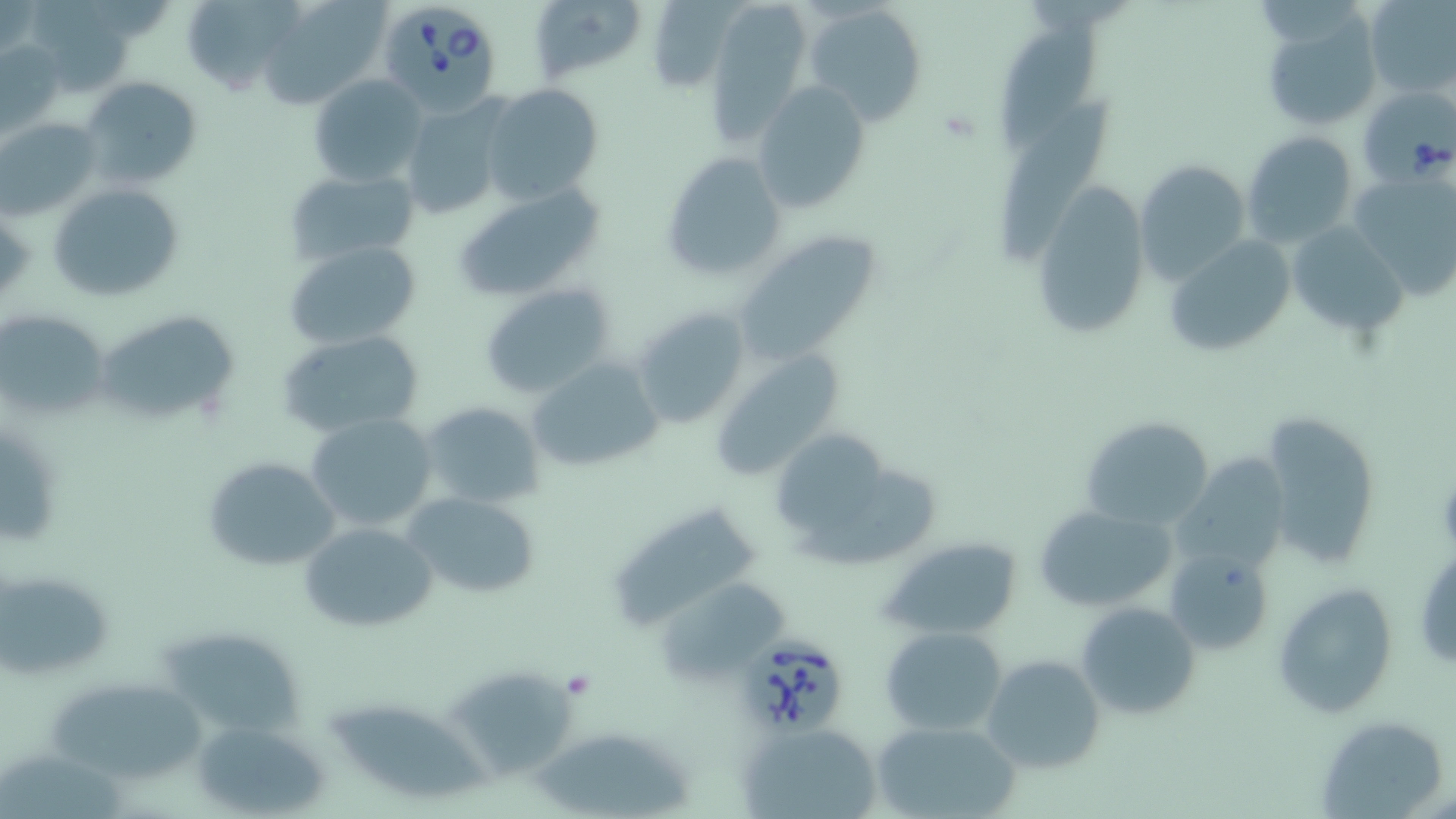

{
  "slide_level_diagnosis": "Babesia divergens",
  "uninfected_red_blood_cell_locations": "approximate bounding boxes as named x1/y1/x2/y2 corners in pixels: (x1=180, y1=0, x2=301, y2=98), (x1=259, y1=0, x2=388, y2=108), (x1=532, y1=0, x2=649, y2=80), (x1=649, y1=0, x2=732, y2=92), (x1=717, y1=0, x2=802, y2=143), (x1=1364, y1=1, x2=1453, y2=99), (x1=805, y1=4, x2=928, y2=128), (x1=1261, y1=11, x2=1383, y2=129), (x1=998, y1=16, x2=1100, y2=149), (x1=2, y1=40, x2=65, y2=133), (x1=306, y1=72, x2=429, y2=186), (x1=80, y1=76, x2=202, y2=188), (x1=753, y1=81, x2=873, y2=214), (x1=479, y1=84, x2=604, y2=206), (x1=1002, y1=96, x2=1116, y2=270), (x1=400, y1=97, x2=512, y2=221), (x1=1, y1=117, x2=100, y2=218), (x1=1242, y1=132, x2=1358, y2=248), (x1=659, y1=152, x2=786, y2=283), (x1=1133, y1=159, x2=1250, y2=284), (x1=1347, y1=167, x2=1456, y2=302), (x1=284, y1=168, x2=419, y2=265), (x1=1031, y1=178, x2=1150, y2=338), (x1=48, y1=180, x2=187, y2=302), (x1=453, y1=182, x2=610, y2=303), (x1=1287, y1=222, x2=1408, y2=338), (x1=733, y1=234, x2=882, y2=366), (x1=1164, y1=234, x2=1296, y2=359), (x1=283, y1=240, x2=419, y2=350), (x1=480, y1=283, x2=615, y2=399), (x1=631, y1=306, x2=752, y2=430), (x1=2, y1=310, x2=108, y2=419), (x1=100, y1=311, x2=239, y2=425), (x1=278, y1=329, x2=425, y2=436), (x1=707, y1=348, x2=848, y2=483), (x1=527, y1=357, x2=663, y2=475), (x1=419, y1=401, x2=549, y2=509), (x1=1258, y1=411, x2=1382, y2=570), (x1=306, y1=412, x2=440, y2=532), (x1=1080, y1=416, x2=1215, y2=530), (x1=778, y1=427, x2=884, y2=531), (x1=201, y1=455, x2=342, y2=572), (x1=1174, y1=455, x2=1291, y2=571), (x1=796, y1=478, x2=945, y2=570), (x1=401, y1=492, x2=542, y2=599), (x1=1032, y1=504, x2=1178, y2=613), (x1=612, y1=509, x2=757, y2=632), (x1=298, y1=522, x2=438, y2=633), (x1=882, y1=538, x2=1027, y2=639), (x1=1167, y1=549, x2=1275, y2=657), (x1=1, y1=571, x2=114, y2=676), (x1=1271, y1=581, x2=1398, y2=717), (x1=1076, y1=601, x2=1201, y2=719), (x1=880, y1=627, x2=1008, y2=736), (x1=164, y1=634, x2=306, y2=737), (x1=982, y1=654, x2=1105, y2=774), (x1=453, y1=669, x2=573, y2=779), (x1=52, y1=684, x2=206, y2=782), (x1=335, y1=704, x2=492, y2=795), (x1=192, y1=715, x2=334, y2=818), (x1=868, y1=719, x2=1021, y2=819), (x1=1316, y1=720, x2=1443, y2=819), (x1=740, y1=723, x2=883, y2=819), (x1=528, y1=731, x2=695, y2=813), (x1=0, y1=750, x2=130, y2=819)",
  "modality": "optical microscopy",
  "image_size": "1456×819 pixels",
  "field_of_view": "one of a larger specimen",
  "stain": "May-Grünwald-Giemsa",
  "magnification": "1000x",
  "preparation": "thin blood smear",
  "babesia_divergens_infected_red_blood_cell_locations": "approximate bounding boxes as named x1/y1/x2/y2 corners in pixels: (x1=377, y1=1, x2=503, y2=117), (x1=1362, y1=83, x2=1455, y2=183), (x1=737, y1=626, x2=848, y2=737)"
}